Point out every Plasmodium parasite.
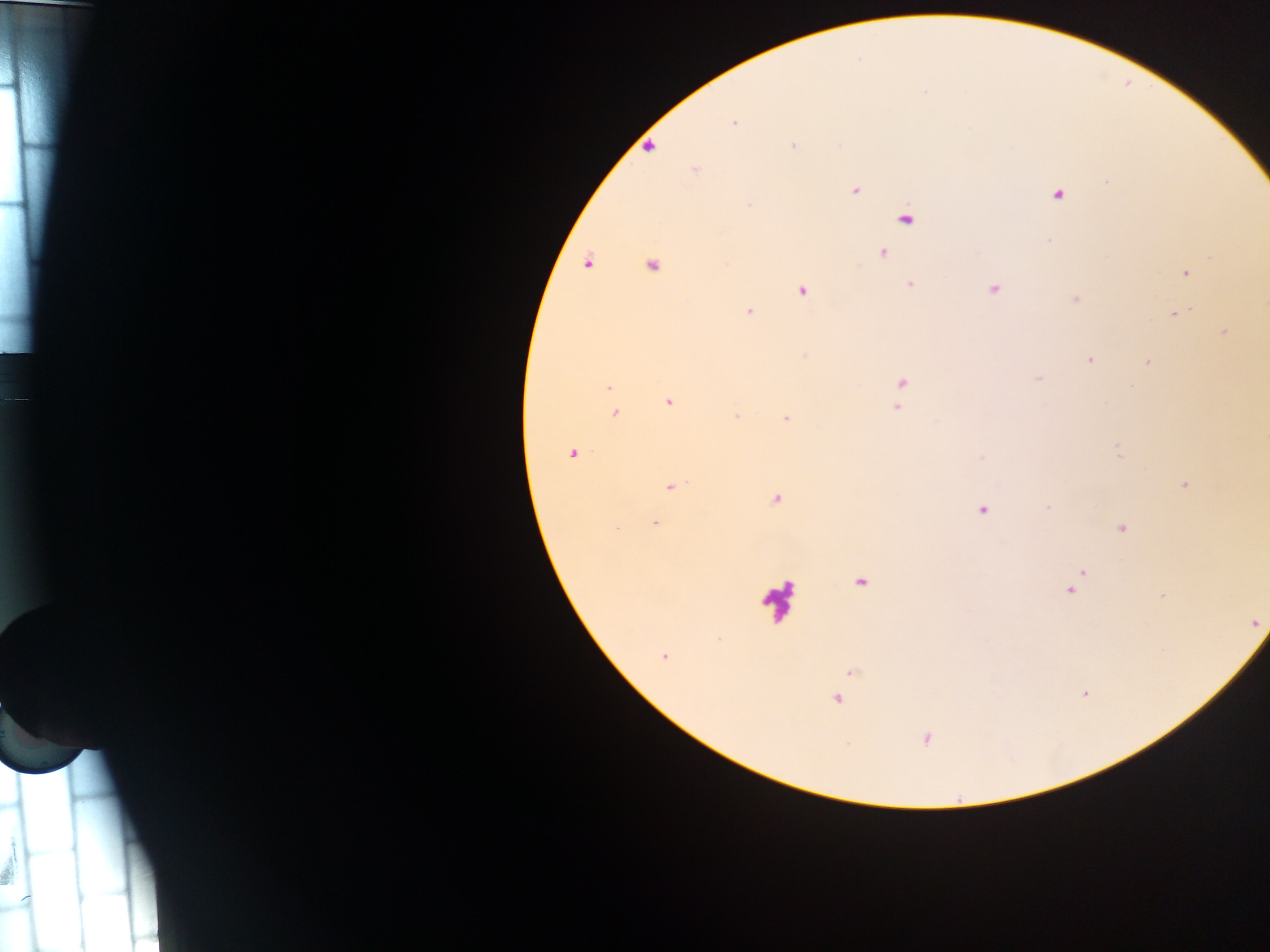
Approximate centers as (x, y) in pixels.
Plasmodium parasites: (733, 123), (839, 144), (793, 145), (650, 147), (695, 169), (856, 190), (1058, 195), (748, 205), (906, 220), (1049, 240), (883, 253), (587, 263), (651, 266), (1186, 273), (910, 285), (994, 289), (801, 291), (1075, 299), (748, 311), (1174, 315), (1224, 333), (805, 356), (1090, 359), (1147, 362), (1038, 378), (902, 384), (609, 387), (1131, 387), (669, 402), (898, 405), (615, 413), (736, 416), (786, 418), (1118, 451), (573, 453), (981, 458), (1185, 484), (672, 486), (776, 499), (1048, 508), (982, 510), (655, 523), (1122, 528), (617, 530), (1077, 578), (861, 583), (1071, 588), (1162, 595), (1256, 622), (664, 656), (850, 672), (1085, 693), (837, 699), (926, 738).

Leukocyte locations: (776, 600). Image is 1270×952 pixels. Thick blood smear. Photographed through a microscope with a mobile-phone camera. Single field of view. Sample from Ghana.